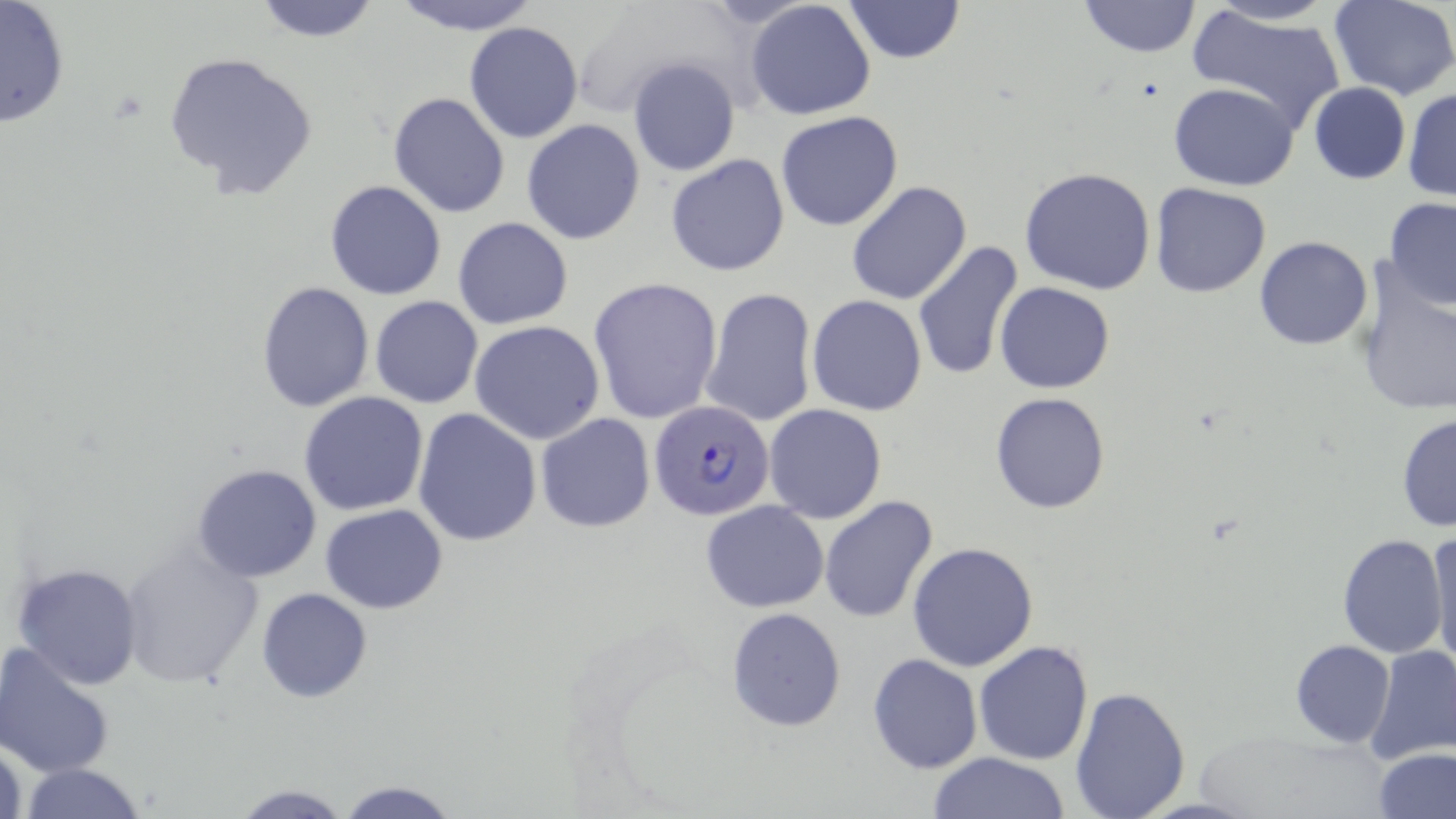

slide-level diagnosis = Plasmodium falciparum
magnification = 1000x
field of view = one of a larger specimen
modality = optical microscopy
Plasmodium falciparum-infected red blood cell locations = approximate bounding boxes as (x1,y1)-(x2,y2) corner pairs in pixels: (650,401)-(774,522)
image size = 1456×819 pixels
uninfected red blood cell locations = approximate bounding boxes as (x1,y1)-(x2,y2) corner pairs in pixels: (251,0)-(384,43), (387,0)-(545,36), (841,0)-(966,64), (1077,0)-(1201,58), (1329,0)-(1456,100), (0,1)-(71,129), (745,1)-(876,119), (1189,5)-(1347,134), (464,21)-(583,143), (162,50)-(320,201), (628,58)-(741,176), (1169,82)-(1299,190), (1308,83)-(1411,185), (1403,87)-(1456,200), (387,91)-(511,218), (776,111)-(903,231), (521,119)-(645,245), (666,153)-(790,276), (1018,167)-(1157,295), (324,180)-(448,300), (845,181)-(972,306), (1149,183)-(1272,298), (1382,197)-(1456,310), (452,217)-(574,330), (1254,237)-(1373,351), (912,240)-(1023,382), (1352,260)-(1456,418), (588,277)-(723,424), (255,280)-(375,412), (992,282)-(1115,393), (701,288)-(817,429), (808,295)-(927,416), (369,296)-(484,409), (470,321)-(604,444), (298,392)-(429,515), (990,392)-(1109,513), (764,404)-(887,523), (413,408)-(543,546), (535,413)-(655,532), (1396,413)-(1455,534), (191,463)-(323,583), (819,495)-(938,624), (701,501)-(829,612), (321,503)-(447,613), (1427,523)-(1456,671), (1336,533)-(1449,658), (908,541)-(1038,671), (118,543)-(263,689), (10,562)-(144,689), (256,587)-(372,703), (727,606)-(846,731), (972,640)-(1095,764), (1289,640)-(1395,748), (1,642)-(118,779), (1364,646)-(1455,765), (867,654)-(981,773), (1067,686)-(1191,819), (0,735)-(26,819), (1374,748)-(1456,818), (928,752)-(1072,819), (16,762)-(151,818), (335,777)-(460,818), (229,782)-(355,818)
preparation = thin blood film
stain = May-Grünwald-Giemsa